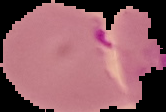 The area outside the segmented cell region is set to black. Image is 166×112 pixels. Malaria status: parasitized. From a thin blood smear.